Describe the morphology of the erythrocytes.
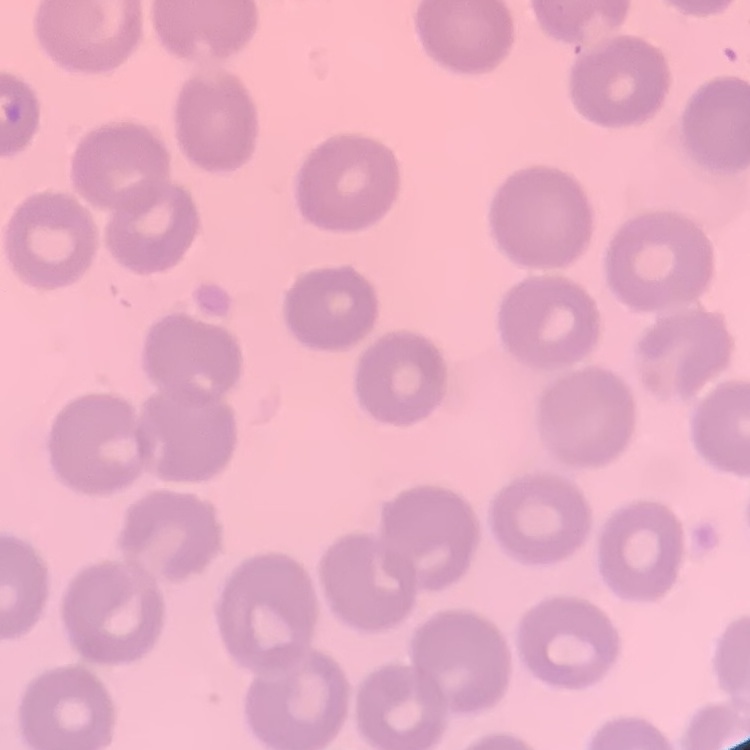

They show no rouleaux formation.

Summary:
  - Image type: square crop of a larger photomicrograph
  - Stain: Field's or Giemsa
  - Preparation: thin blood film